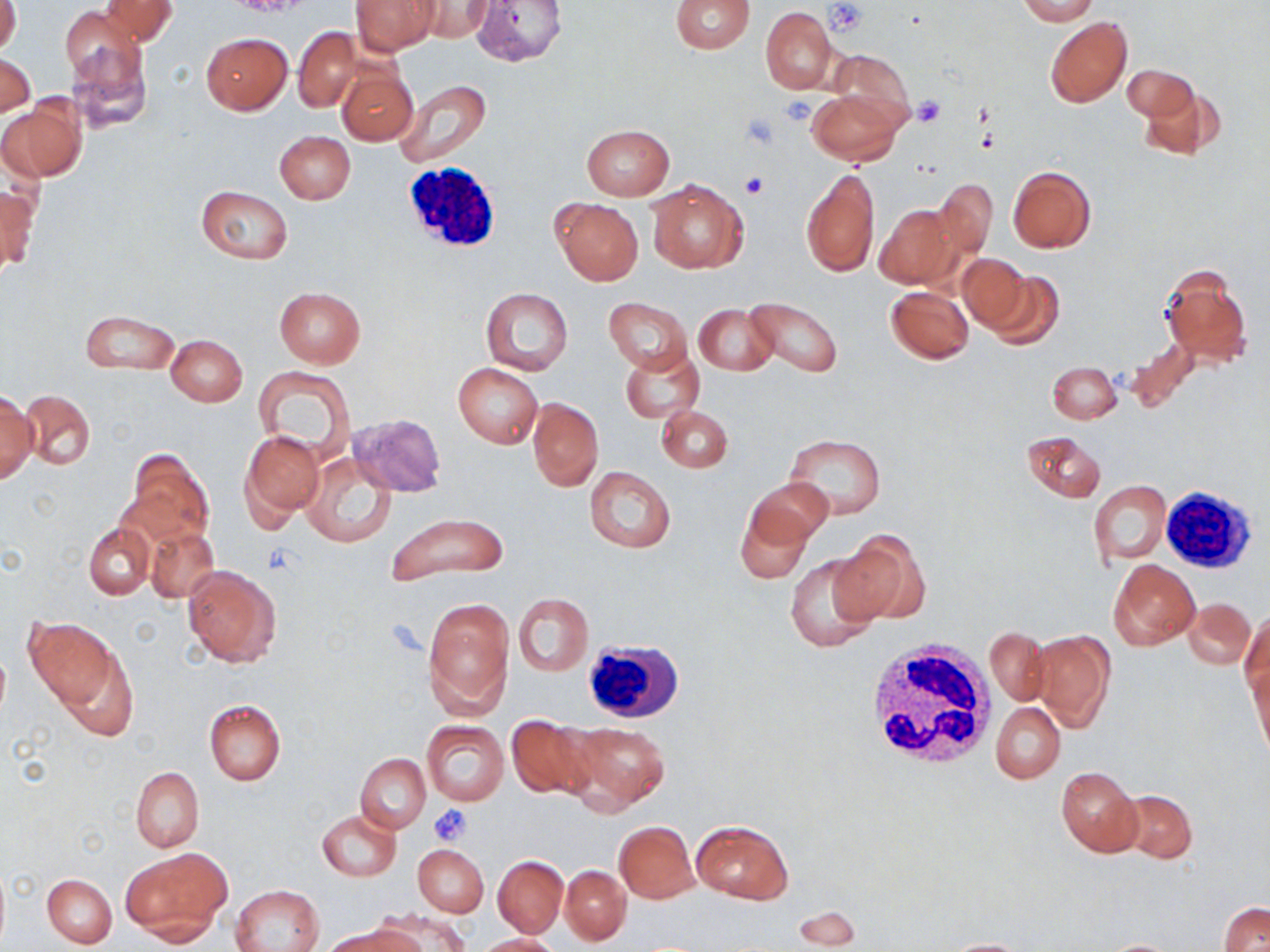

slide_level_diagnosis: negative for blood parasites
platelet_locations: 'approximate bounding boxes as named x1/y1/x2/y2 corners in pixels: (x1=826, y1=1, x2=868, y2=36), (x1=780, y1=94, x2=817, y2=125), (x1=914, y1=97, x2=945, y2=127), (x1=741, y1=113, x2=781, y2=149), (x1=741, y1=173, x2=767, y2=199), (x1=260, y1=543, x2=299, y2=577), (x1=428, y1=803, x2=470, y2=844)'
field_of_view: single
modality: optical microscopy
image_size: 1270×952 pixels
white_blood_cell_locations: 'approximate bounding boxes as named x1/y1/x2/y2 corners in pixels: (x1=399, y1=162, x2=504, y2=256), (x1=1156, y1=484, x2=1259, y2=575), (x1=864, y1=640, x2=997, y2=771), (x1=588, y1=642, x2=696, y2=722)'
uninfected_red_blood_cell_locations: 'approximate bounding boxes as named x1/y1/x2/y2 corners in pixels: (x1=0, y1=0, x2=21, y2=57), (x1=99, y1=0, x2=177, y2=45), (x1=352, y1=0, x2=439, y2=56), (x1=411, y1=0, x2=494, y2=42), (x1=469, y1=0, x2=572, y2=68), (x1=670, y1=0, x2=753, y2=54), (x1=1019, y1=0, x2=1098, y2=24), (x1=761, y1=7, x2=836, y2=94), (x1=61, y1=8, x2=144, y2=90), (x1=1044, y1=17, x2=1132, y2=107), (x1=292, y1=27, x2=364, y2=112), (x1=66, y1=31, x2=154, y2=134), (x1=201, y1=32, x2=293, y2=114), (x1=830, y1=50, x2=916, y2=133), (x1=0, y1=53, x2=36, y2=119), (x1=1121, y1=64, x2=1196, y2=121), (x1=338, y1=67, x2=417, y2=145), (x1=394, y1=81, x2=491, y2=168), (x1=1139, y1=82, x2=1227, y2=163), (x1=809, y1=90, x2=903, y2=164), (x1=1, y1=99, x2=84, y2=181), (x1=580, y1=124, x2=675, y2=200), (x1=274, y1=130, x2=355, y2=203), (x1=1008, y1=166, x2=1095, y2=252), (x1=801, y1=167, x2=879, y2=279), (x1=647, y1=178, x2=748, y2=273), (x1=933, y1=180, x2=997, y2=258), (x1=0, y1=184, x2=38, y2=275), (x1=195, y1=186, x2=293, y2=263), (x1=551, y1=198, x2=643, y2=285), (x1=873, y1=204, x2=959, y2=288), (x1=957, y1=253, x2=1031, y2=332), (x1=1159, y1=264, x2=1252, y2=370), (x1=981, y1=271, x2=1065, y2=351), (x1=885, y1=285, x2=973, y2=364), (x1=274, y1=287, x2=366, y2=368), (x1=481, y1=288, x2=573, y2=374), (x1=605, y1=297, x2=692, y2=373), (x1=745, y1=297, x2=843, y2=378), (x1=693, y1=303, x2=779, y2=375), (x1=81, y1=310, x2=179, y2=374), (x1=166, y1=335, x2=246, y2=405), (x1=621, y1=348, x2=704, y2=422), (x1=1047, y1=361, x2=1121, y2=423), (x1=453, y1=364, x2=542, y2=448), (x1=253, y1=366, x2=356, y2=461), (x1=22, y1=390, x2=96, y2=470), (x1=0, y1=392, x2=37, y2=483), (x1=528, y1=398, x2=603, y2=491), (x1=656, y1=406, x2=733, y2=472), (x1=347, y1=413, x2=447, y2=497), (x1=240, y1=429, x2=324, y2=525), (x1=1023, y1=430, x2=1106, y2=502), (x1=784, y1=434, x2=887, y2=517), (x1=124, y1=450, x2=213, y2=548), (x1=301, y1=454, x2=397, y2=548), (x1=585, y1=468, x2=675, y2=553), (x1=746, y1=476, x2=833, y2=550), (x1=1090, y1=481, x2=1170, y2=564), (x1=734, y1=502, x2=812, y2=584), (x1=385, y1=512, x2=509, y2=584), (x1=84, y1=523, x2=154, y2=599), (x1=146, y1=525, x2=218, y2=603), (x1=834, y1=530, x2=929, y2=625), (x1=784, y1=552, x2=882, y2=653), (x1=1110, y1=559, x2=1199, y2=649), (x1=182, y1=565, x2=282, y2=667), (x1=513, y1=594, x2=592, y2=675), (x1=422, y1=595, x2=514, y2=718), (x1=1186, y1=599, x2=1254, y2=668), (x1=1241, y1=609, x2=1269, y2=697), (x1=24, y1=618, x2=116, y2=706), (x1=985, y1=628, x2=1051, y2=705), (x1=1030, y1=630, x2=1114, y2=731), (x1=57, y1=646, x2=137, y2=741), (x1=1248, y1=658, x2=1269, y2=758), (x1=204, y1=698, x2=286, y2=784), (x1=990, y1=702, x2=1066, y2=783), (x1=506, y1=716, x2=594, y2=799), (x1=421, y1=720, x2=508, y2=804), (x1=565, y1=721, x2=670, y2=813), (x1=355, y1=754, x2=431, y2=832), (x1=131, y1=766, x2=204, y2=852), (x1=1055, y1=766, x2=1141, y2=857), (x1=1118, y1=788, x2=1197, y2=863), (x1=317, y1=810, x2=401, y2=881), (x1=691, y1=819, x2=792, y2=904), (x1=614, y1=821, x2=699, y2=903), (x1=413, y1=843, x2=488, y2=916), (x1=123, y1=849, x2=228, y2=940), (x1=492, y1=855, x2=567, y2=937), (x1=0, y1=865, x2=10, y2=949), (x1=560, y1=865, x2=631, y2=945), (x1=43, y1=873, x2=117, y2=948), (x1=232, y1=885, x2=324, y2=952), (x1=1219, y1=902, x2=1270, y2=952), (x1=791, y1=904, x2=862, y2=949), (x1=376, y1=910, x2=470, y2=952), (x1=335, y1=923, x2=423, y2=952), (x1=476, y1=933, x2=560, y2=952), (x1=939, y1=937, x2=1034, y2=951), (x1=1096, y1=938, x2=1188, y2=951)'
magnification: 1000x
stain: May-Grünwald-Giemsa
preparation: thin blood film